Assess this cell for malaria.
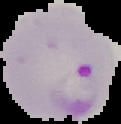

It is parasitized.

{
  "image_size": "121×124 pixels",
  "image_type": "segmented cell region on a black background",
  "preparation": "thin blood smear"
}